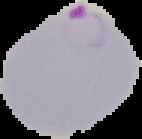

From a thin blood smear. Image is 142×139 pixels. The area outside the segmented cell region is set to black. Malaria status: parasitized.